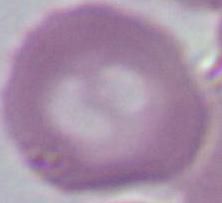
Summary:
  - Identification: red blood cell
  - Modality: micrograph
  - Magnification: 1000x